Give the position of every Plasmodium parasite visible.
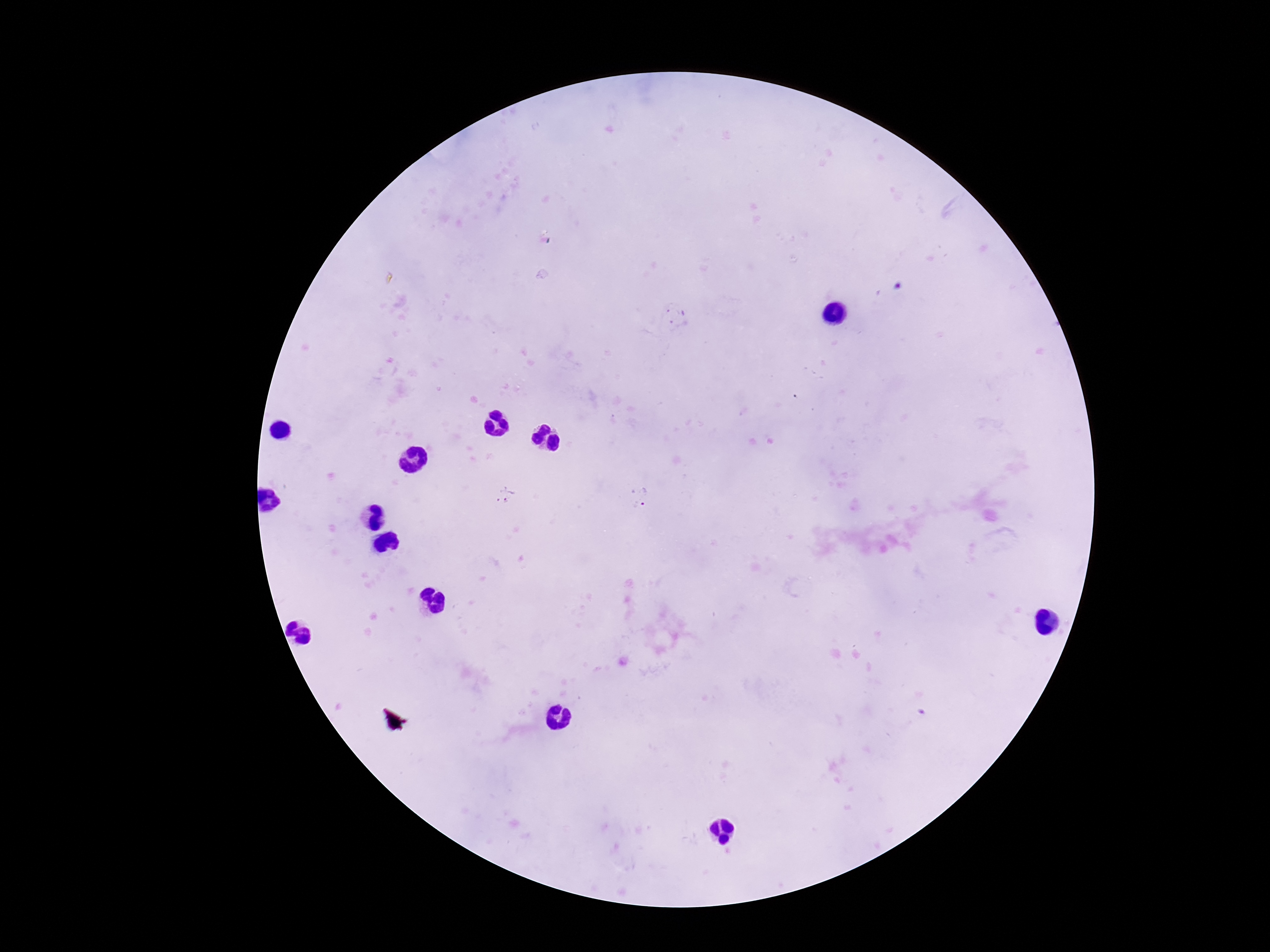
Approximate centers as {x, y} in pixels.
Plasmodium parasites: {675, 317}, {505, 496}, {641, 497}.

Single field of view. Photographed through the microscope eyepiece with a smartphone camera. Image is 1270×952 pixels. Thick peripheral-blood smear. 100x magnification. Patient malaria status: positive. Giemsa-stained preparation.